Identify the parasite.
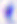

This is Toxoplasma gondii.

Captured at 400x magnification. Photomicrograph.